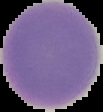
Image is 103×112 pixels. The area outside the segmented cell region is set to black. From a thin blood smear. Malaria status: uninfected.